Identify the blood parasite species.
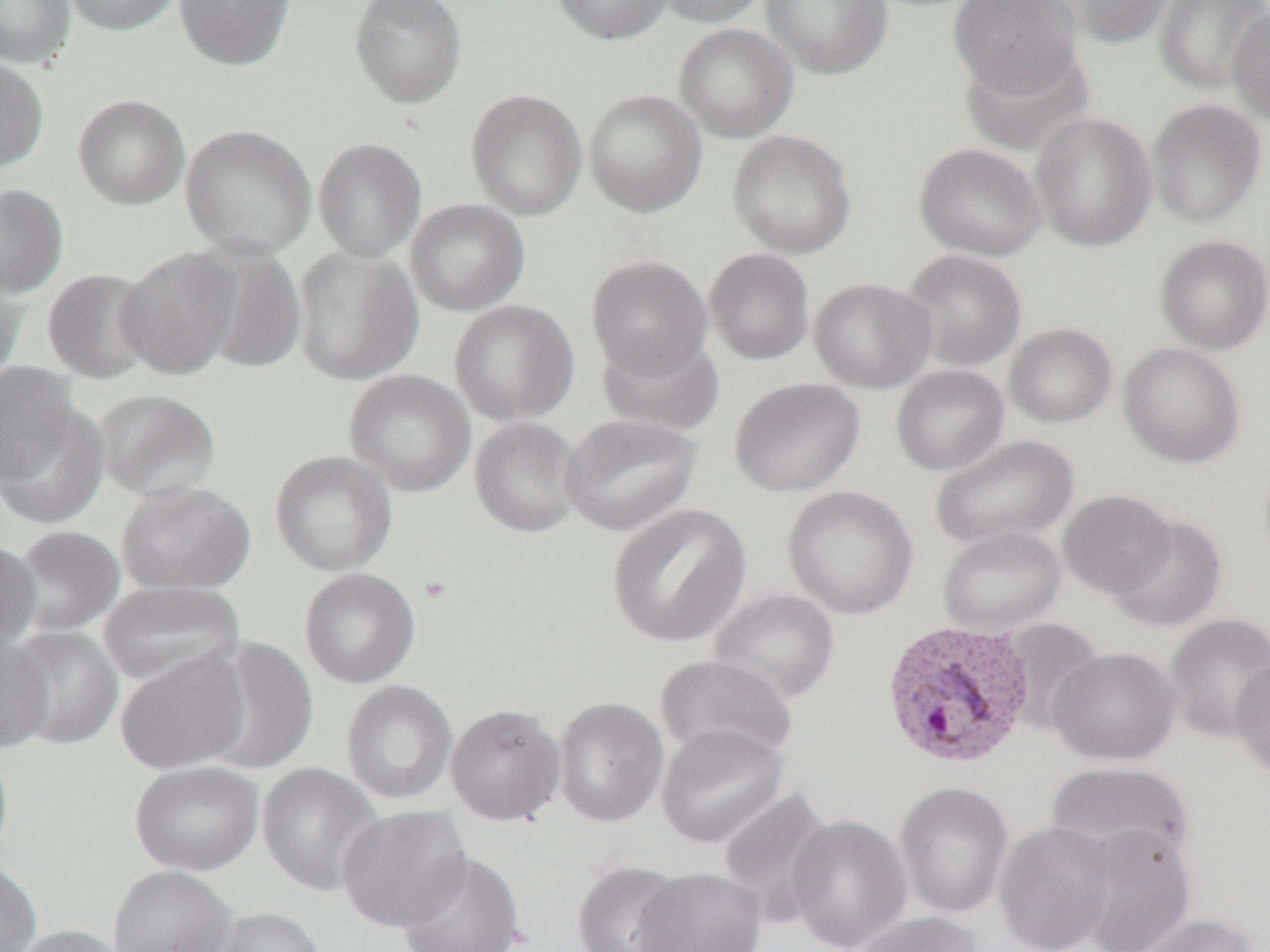

Plasmodium vivax.

field of view = one of a larger specimen
magnification = 1000x
image size = 1270×952 pixels
Plasmodium vivax-infected red blood cell locations = approximate bounding boxes as (x1,y1)-(x2,y2) corner pairs in pixels: (880,619)-(1037,769)
uninfected red blood cell locations = approximate bounding boxes as (x1,y1)-(x2,y2) corner pairs in pixels: (0,0)-(76,67), (61,0)-(183,37), (173,0)-(297,71), (349,0)-(467,108), (551,0)-(674,46), (654,0)-(770,26), (761,0)-(893,80), (1057,0)-(1175,48), (1154,0)-(1270,95), (949,1)-(1083,98), (1227,6)-(1270,127), (673,23)-(799,143), (957,44)-(1094,155), (0,54)-(50,174), (465,88)-(588,221), (584,89)-(708,217), (72,93)-(191,210), (1146,99)-(1266,228), (1030,111)-(1157,251), (180,123)-(317,259), (727,129)-(857,258), (312,137)-(427,262), (914,143)-(1046,261), (0,183)-(69,299), (406,198)-(530,316), (1155,235)-(1270,355), (192,243)-(308,376), (292,245)-(424,386), (116,246)-(242,380), (704,248)-(815,364), (901,250)-(1027,371), (586,254)-(713,378), (0,268)-(29,388), (41,268)-(158,384), (809,277)-(936,393), (449,299)-(579,426), (1004,323)-(1117,428), (596,332)-(725,435), (1119,341)-(1246,469), (891,364)-(1010,476), (344,368)-(476,497), (730,377)-(866,497), (0,384)-(108,528), (94,388)-(222,504), (560,412)-(702,536), (469,416)-(586,538), (930,434)-(1079,552), (269,449)-(398,576), (115,480)-(256,595), (783,485)-(919,619), (1058,489)-(1176,598), (608,503)-(751,648), (1107,514)-(1228,633), (11,525)-(127,636), (938,525)-(1067,636), (0,539)-(41,655), (299,567)-(420,689), (97,580)-(246,690), (708,587)-(840,705), (1163,612)-(1270,744), (998,617)-(1105,733), (3,625)-(124,750), (200,636)-(319,775), (0,637)-(54,754), (1049,647)-(1182,765), (114,650)-(251,775), (654,654)-(798,766), (1231,654)-(1270,781), (341,680)-(458,805), (553,697)-(669,827), (445,704)-(566,825), (657,724)-(788,849), (0,740)-(14,867), (129,761)-(264,876), (1045,761)-(1195,868), (257,762)-(387,897), (893,781)-(1014,919), (718,785)-(836,928), (336,805)-(472,932), (787,814)-(913,952), (994,821)-(1117,952), (1071,826)-(1197,952), (396,850)-(525,952), (0,860)-(43,952), (572,860)-(691,952), (107,864)-(238,952), (633,868)-(768,952), (199,906)-(326,952), (851,911)-(984,952), (1133,913)-(1261,952), (8,924)-(130,952)
modality = optical microscopy
preparation = thin blood film